Comment on the morphology of the erythrocytes.
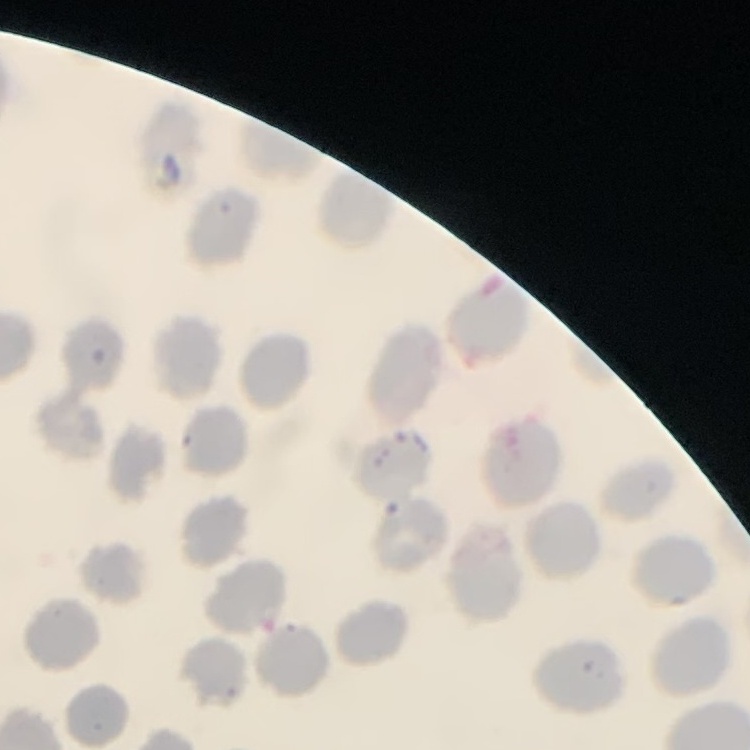

They show no rouleaux formation.

image type = one tile cut from a larger photomicrograph
stain = Field's or Giemsa
preparation = thin blood film